Assess this cell for malaria.
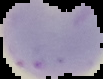
It is parasitized.

image size = 103×79 pixels
image type = cell region segmented out of the field of view; surrounding area masked to black
preparation = thin blood smear